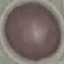
Summary:
  - Result: no malaria parasites seen
  - Capture: smartphone camera at the microscope eyepiece
  - Stain: Giemsa
  - Image type: automatically extracted cell patch, resized to 64 × 64 pixels
  - Preparation: thin smear